Point out every Plasmodium parasite.
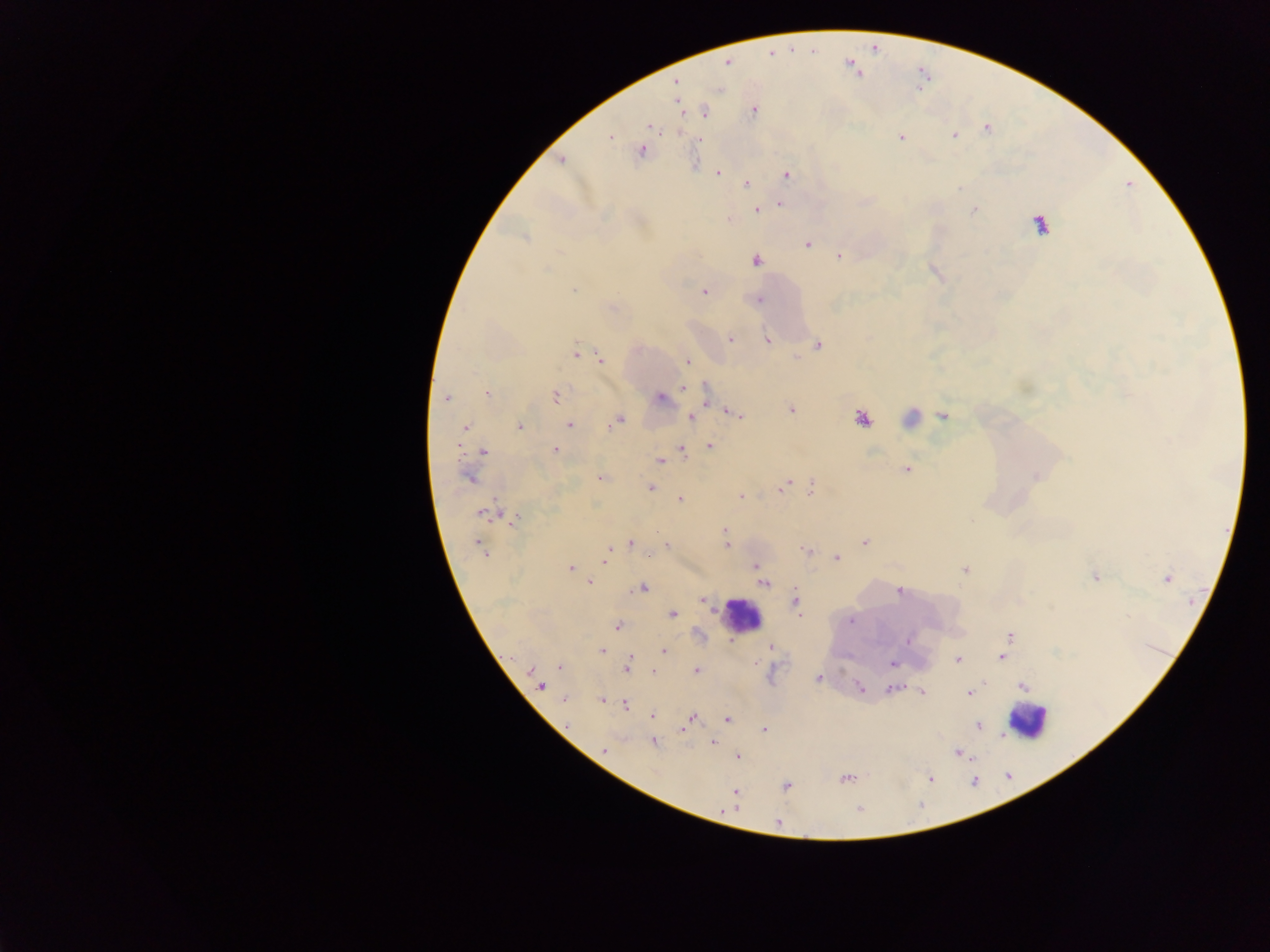
Approximate centers as {x, y} in pixels.
Plasmodium parasites: {727, 63}, {677, 82}, {753, 110}, {705, 113}, {649, 126}, {987, 130}, {954, 135}, {610, 136}, {901, 137}, {701, 139}, {641, 151}, {561, 161}, {718, 173}, {787, 175}, {747, 184}, {780, 205}, {756, 210}, {974, 210}, {728, 220}, {1040, 224}, {524, 238}, {807, 245}, {839, 256}, {756, 260}, {573, 290}, {704, 292}, {758, 299}, {731, 340}, {767, 341}, {818, 344}, {576, 352}, {600, 359}, {687, 361}, {684, 388}, {705, 393}, {487, 395}, {556, 395}, {446, 398}, {661, 398}, {791, 409}, {735, 414}, {943, 415}, {690, 417}, {861, 418}, {618, 420}, {569, 424}, {519, 426}, {465, 428}, {458, 445}, {709, 446}, {682, 449}, {555, 450}, {483, 451}, {661, 461}, {905, 469}, {1034, 476}, {468, 477}, {600, 479}, {650, 488}, {783, 488}, {811, 490}, {741, 497}, {679, 499}, {483, 513}, {513, 520}, {725, 530}, {865, 542}, {631, 543}, {667, 545}, {726, 545}, {479, 546}, {483, 550}, {805, 550}, {608, 553}, {648, 555}, {837, 558}, {605, 560}, {755, 565}, {570, 568}, {964, 570}, {1095, 577}, {1167, 578}, {589, 582}, {764, 583}, {642, 588}, {899, 591}, {796, 600}, {703, 601}, {672, 614}, {799, 615}, {851, 620}, {617, 626}, {1010, 636}, {906, 641}, {771, 647}, {1007, 647}, {602, 651}, {664, 652}, {629, 656}, {1002, 657}, {958, 660}, {892, 664}, {559, 667}, {627, 668}, {531, 670}, {696, 671}, {653, 672}, {818, 678}, {541, 686}, {860, 687}, {1023, 687}, {892, 689}, {922, 692}, {969, 693}, {564, 699}, {602, 700}, {625, 704}, {652, 715}, {692, 718}, {727, 719}, {567, 725}, {978, 726}, {682, 730}, {764, 730}, {712, 742}, {653, 743}, {604, 750}, {957, 753}, {738, 756}, {846, 778}, {929, 778}, {786, 786}, {735, 792}, {728, 809}, {859, 809}, {777, 821}.

Leukocyte locations: {911, 416}, {741, 616}, {1027, 721}. Photographed through a microscope with a mobile-phone camera. Sample from Ghana. Thick blood film. Single field of view. Image is 1270×952 pixels.